Name the cell type shown.
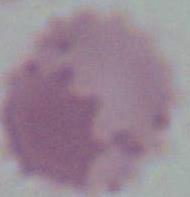

This is an erythrocyte.

1000x magnification. Micrograph.